Describe the morphology of the erythrocytes.
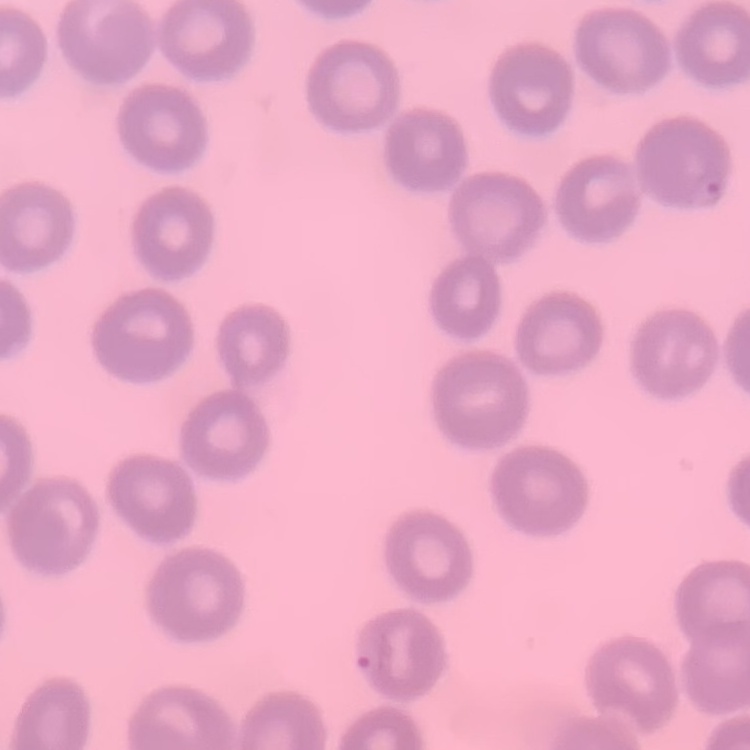
No rouleaux formation.

Summary:
  - Stain: Field's or Giemsa
  - Image type: one tile cut from a larger photomicrograph
  - Preparation: thin peripheral smear